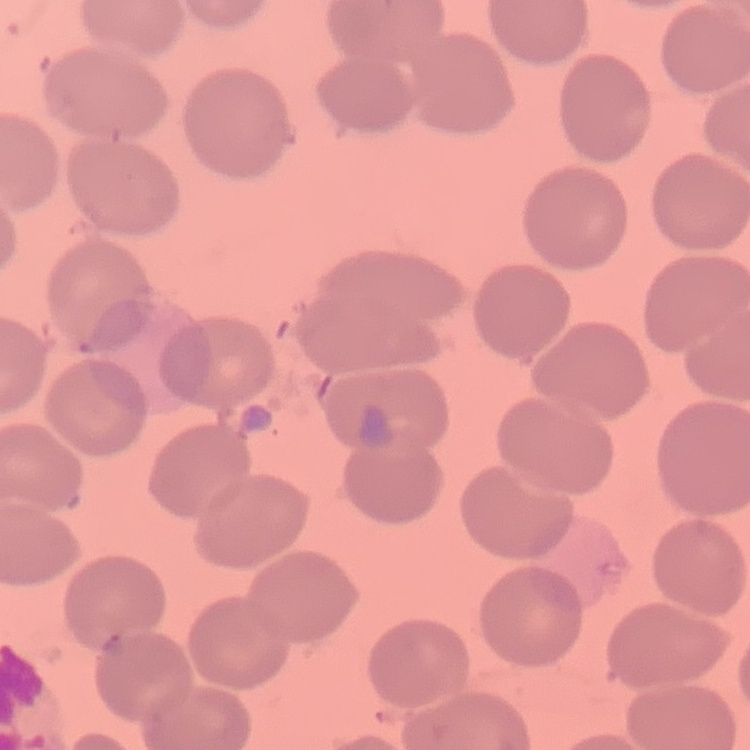

Summary:
  - Erythrocyte morphology: no rouleaux formation
  - Stain: Field's or Giemsa
  - Image type: square crop of a larger photomicrograph
  - Preparation: thin blood smear